Locate every blood parasite and identify its species.
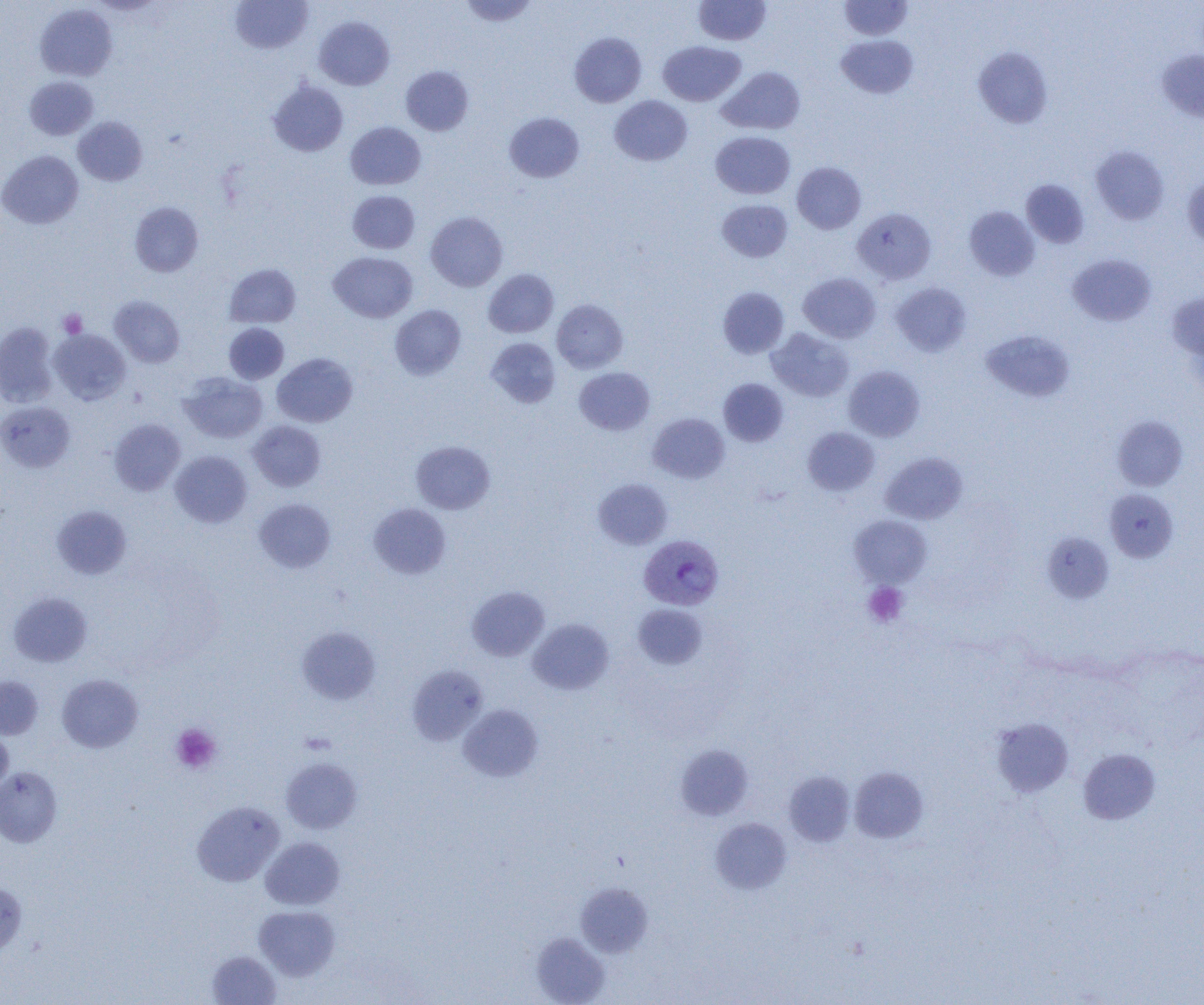

Approximate bounding boxes as named x1/y1/x2/y2 corners in pixels.
Plasmodium vivax-infected red blood cells: (x1=639, y1=534, x2=723, y2=610).
No Plasmodium falciparum, Plasmodium ovale, Plasmodium malariae, Babesia divergens, or Trypanosoma brucei observed.

slide-level diagnosis = Plasmodium vivax
image size = 1204×1005 pixels
magnification = 1000x
platelet locations = approximate bounding boxes as named x1/y1/x2/y2 corners in pixels: (x1=58, y1=309, x2=87, y2=337), (x1=863, y1=582, x2=908, y2=627), (x1=170, y1=723, x2=221, y2=774)
field of view = one of a larger specimen
modality = optical microscopy
preparation = thin blood smear
uninfected red blood cell locations = approximate bounding boxes as named x1/y1/x2/y2 corners in pixels: (x1=458, y1=0, x2=538, y2=27), (x1=693, y1=0, x2=770, y2=46), (x1=838, y1=0, x2=913, y2=40), (x1=230, y1=1, x2=313, y2=54), (x1=35, y1=4, x2=117, y2=81), (x1=314, y1=16, x2=394, y2=90), (x1=569, y1=32, x2=646, y2=107), (x1=836, y1=34, x2=918, y2=99), (x1=658, y1=41, x2=746, y2=106), (x1=973, y1=47, x2=1053, y2=128), (x1=1157, y1=49, x2=1204, y2=123), (x1=400, y1=65, x2=474, y2=136), (x1=718, y1=66, x2=805, y2=135), (x1=24, y1=76, x2=98, y2=140), (x1=268, y1=80, x2=348, y2=157), (x1=610, y1=95, x2=692, y2=166), (x1=504, y1=112, x2=584, y2=183), (x1=73, y1=116, x2=148, y2=186), (x1=345, y1=121, x2=426, y2=190), (x1=711, y1=131, x2=795, y2=199), (x1=1090, y1=145, x2=1169, y2=225), (x1=0, y1=150, x2=83, y2=229), (x1=791, y1=162, x2=866, y2=234), (x1=1182, y1=173, x2=1204, y2=249), (x1=1021, y1=179, x2=1089, y2=248), (x1=348, y1=190, x2=419, y2=253), (x1=716, y1=199, x2=792, y2=262), (x1=130, y1=201, x2=203, y2=276), (x1=964, y1=206, x2=1040, y2=281), (x1=852, y1=208, x2=936, y2=284), (x1=426, y1=211, x2=507, y2=291), (x1=328, y1=252, x2=418, y2=322), (x1=1068, y1=254, x2=1156, y2=326), (x1=224, y1=264, x2=301, y2=328), (x1=483, y1=269, x2=559, y2=338), (x1=798, y1=272, x2=880, y2=343), (x1=891, y1=282, x2=971, y2=356), (x1=718, y1=287, x2=789, y2=358), (x1=1167, y1=291, x2=1204, y2=367), (x1=109, y1=296, x2=184, y2=367), (x1=552, y1=300, x2=627, y2=373), (x1=390, y1=304, x2=466, y2=380), (x1=0, y1=322, x2=59, y2=407), (x1=223, y1=323, x2=289, y2=384), (x1=767, y1=328, x2=854, y2=402), (x1=49, y1=329, x2=131, y2=404), (x1=980, y1=329, x2=1076, y2=402), (x1=486, y1=337, x2=561, y2=408), (x1=272, y1=353, x2=358, y2=427), (x1=843, y1=365, x2=925, y2=441), (x1=574, y1=367, x2=655, y2=435), (x1=179, y1=372, x2=267, y2=443), (x1=718, y1=378, x2=788, y2=445), (x1=0, y1=401, x2=76, y2=473), (x1=648, y1=412, x2=729, y2=483), (x1=1112, y1=415, x2=1188, y2=491), (x1=109, y1=419, x2=185, y2=495), (x1=248, y1=420, x2=325, y2=491), (x1=802, y1=427, x2=880, y2=496), (x1=411, y1=441, x2=495, y2=514), (x1=170, y1=450, x2=252, y2=528), (x1=881, y1=452, x2=967, y2=524), (x1=593, y1=478, x2=673, y2=549), (x1=1104, y1=488, x2=1178, y2=563), (x1=253, y1=498, x2=335, y2=573), (x1=368, y1=502, x2=451, y2=579), (x1=52, y1=505, x2=132, y2=579), (x1=849, y1=515, x2=932, y2=587), (x1=1042, y1=532, x2=1114, y2=603), (x1=467, y1=586, x2=549, y2=661), (x1=8, y1=592, x2=92, y2=667), (x1=633, y1=604, x2=707, y2=669), (x1=528, y1=618, x2=614, y2=694), (x1=297, y1=625, x2=381, y2=705), (x1=408, y1=665, x2=487, y2=745), (x1=56, y1=673, x2=143, y2=753), (x1=0, y1=676, x2=43, y2=739), (x1=458, y1=704, x2=543, y2=781), (x1=991, y1=717, x2=1073, y2=797), (x1=0, y1=729, x2=13, y2=795), (x1=675, y1=743, x2=753, y2=820), (x1=1078, y1=748, x2=1160, y2=824), (x1=281, y1=757, x2=362, y2=834), (x1=0, y1=767, x2=62, y2=847), (x1=849, y1=767, x2=928, y2=843), (x1=784, y1=771, x2=855, y2=847), (x1=191, y1=801, x2=285, y2=886), (x1=710, y1=818, x2=791, y2=894), (x1=260, y1=837, x2=344, y2=910), (x1=576, y1=882, x2=653, y2=957), (x1=0, y1=883, x2=27, y2=954), (x1=254, y1=905, x2=339, y2=980), (x1=532, y1=932, x2=610, y2=1005), (x1=207, y1=950, x2=281, y2=1004)